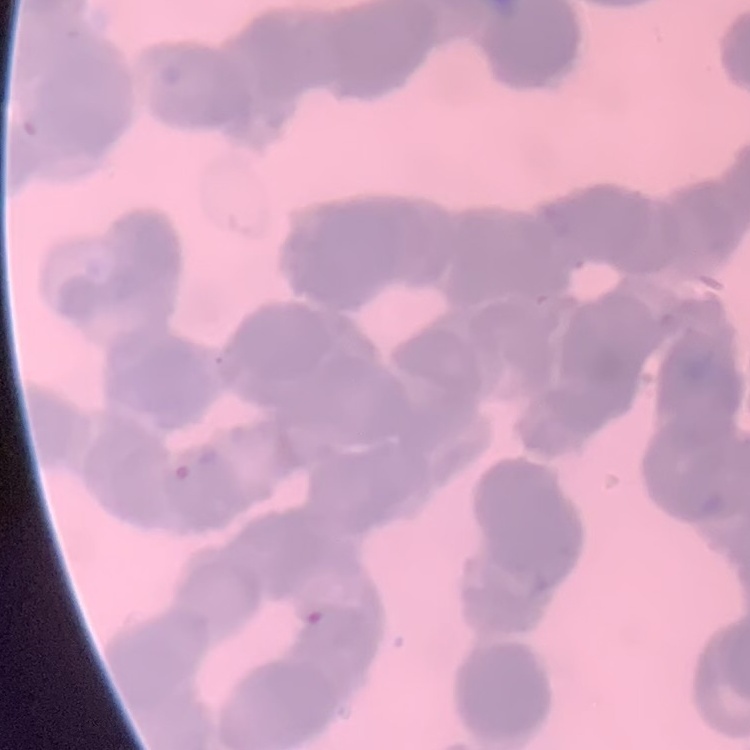
erythrocyte morphology = rouleaux formation
image type = one tile cut from a larger photomicrograph
preparation = thin blood smear
stain = Field's or Giemsa